Locate every Plasmodium parasite.
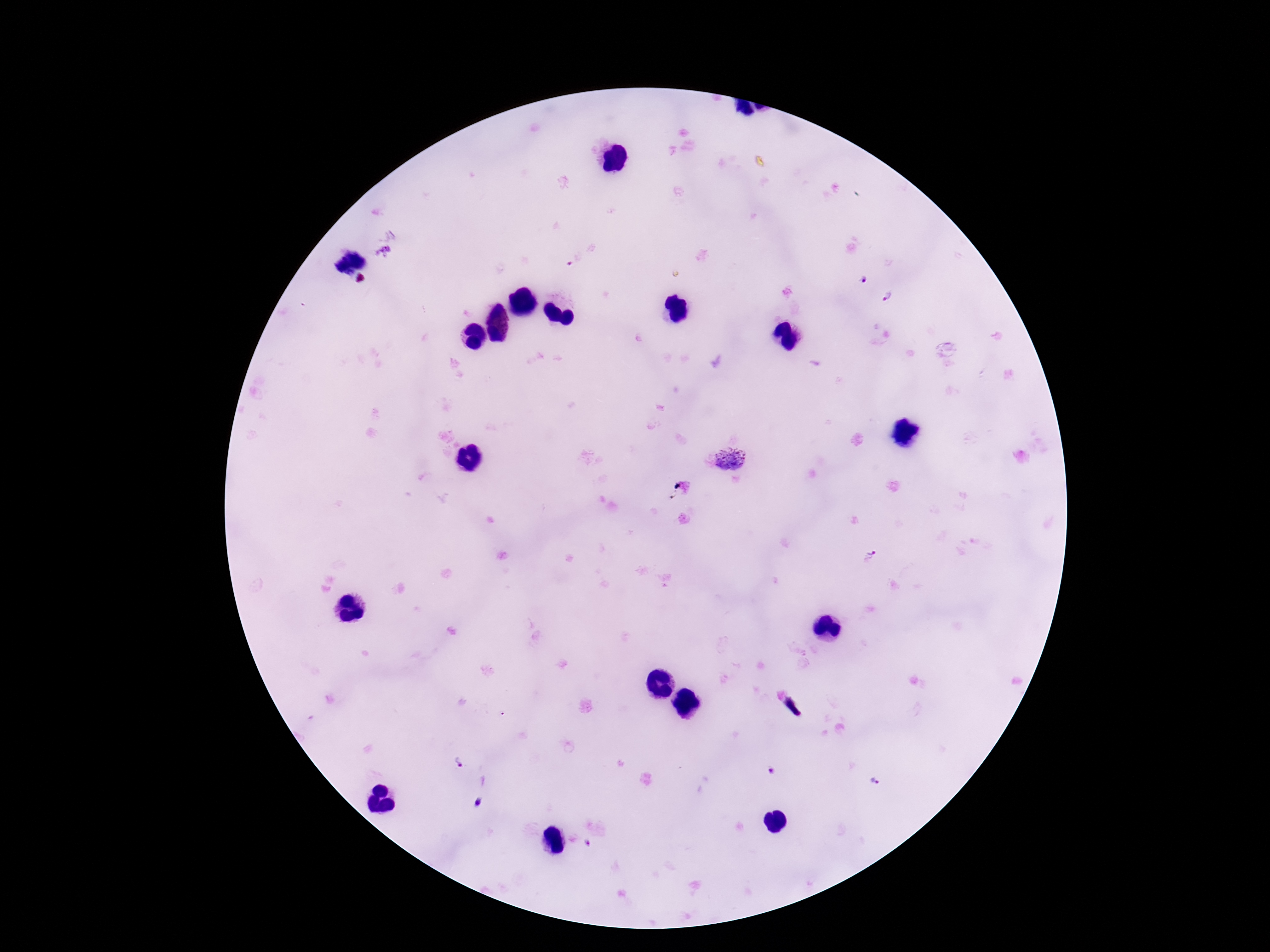
Approximate centers as {x, y} in pixels.
Plasmodium parasites: {383, 253}, {862, 279}, {889, 298}, {729, 459}, {871, 554}, {458, 762}, {772, 772}, {874, 782}, {589, 844}.

Smartphone photograph taken through the microscope eyepiece. Patient malaria status: infected. Single field of view. Image is 1270×952 pixels. Thick peripheral-blood smear. Giemsa-stained preparation. 100x magnification.